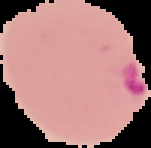

image size = 151×148 pixels
malaria status = parasitized
preparation = thin blood film
image type = segmented cell region on a black background